State the preparation type.
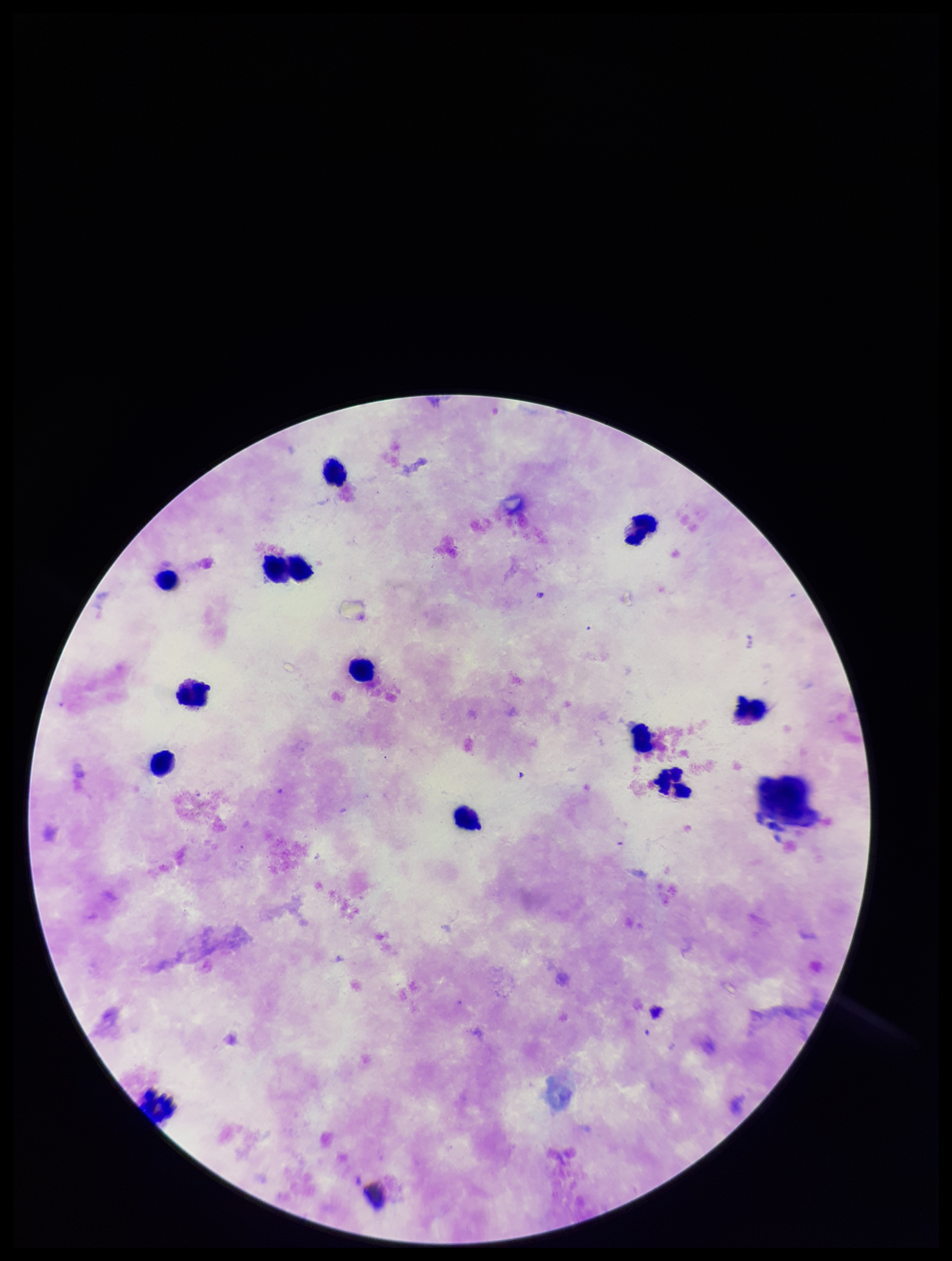
It is a thick blood smear.

{
  "plasmodium_parasites": "none detected",
  "parasite_count": 0,
  "image_size": "952×1261 pixels",
  "leukocyte_count": 12,
  "patient_malaria_status": "negative",
  "stain": "Giemsa",
  "field_of_view": "one from this slide",
  "capture": "smartphone photograph through the microscope eyepiece"
}